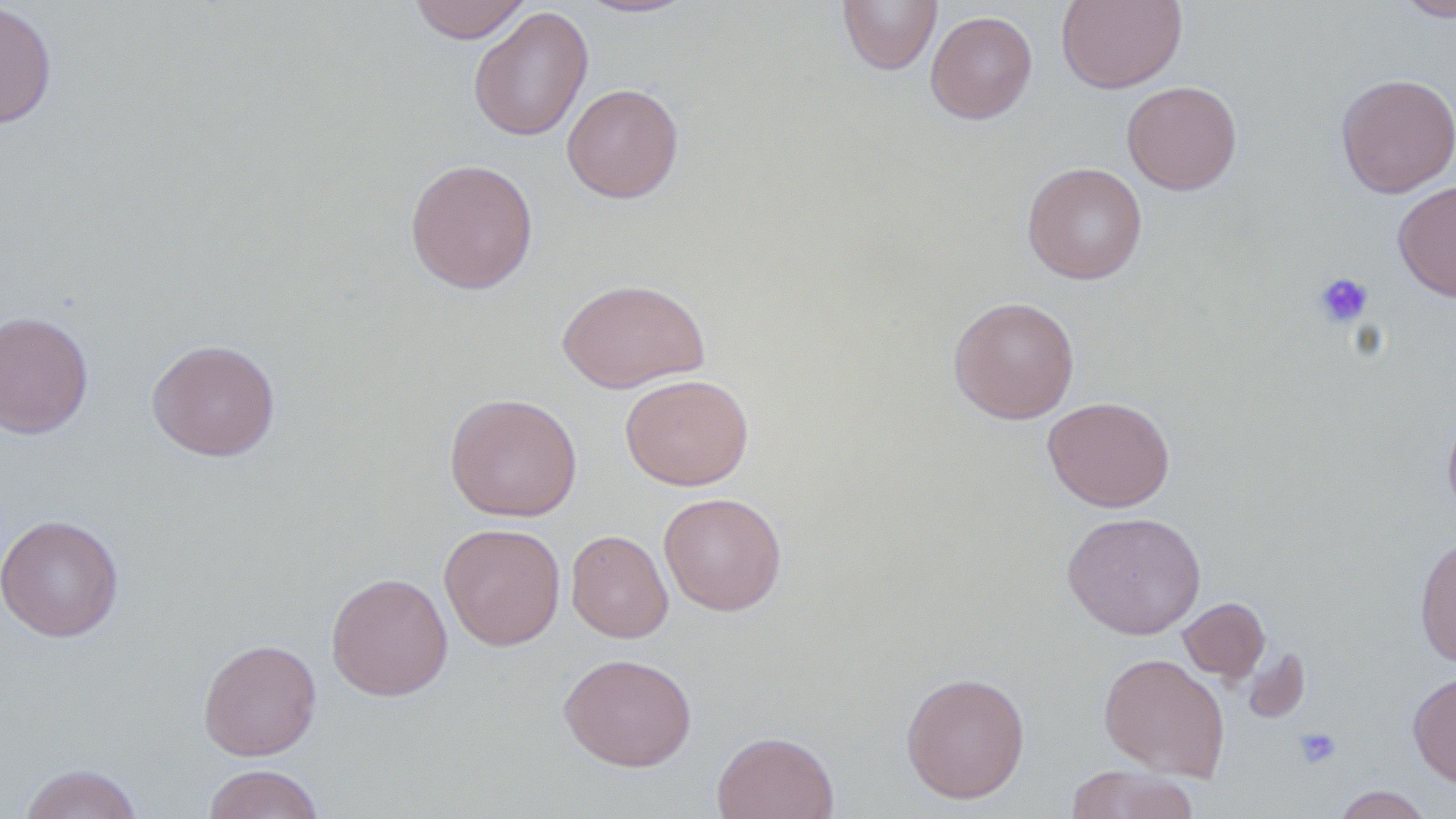 Approximate bounding boxes as named x1/y1/x2/y2 corners in pixels. Uninfected red blood cell locations: (x1=408, y1=0, x2=531, y2=43), (x1=574, y1=0, x2=699, y2=19), (x1=837, y1=0, x2=942, y2=75), (x1=1056, y1=0, x2=1187, y2=93), (x1=1396, y1=0, x2=1456, y2=22), (x1=0, y1=1, x2=57, y2=129), (x1=468, y1=6, x2=594, y2=142), (x1=925, y1=10, x2=1038, y2=124), (x1=1335, y1=73, x2=1456, y2=198), (x1=1122, y1=80, x2=1242, y2=195), (x1=562, y1=83, x2=684, y2=203), (x1=404, y1=158, x2=539, y2=294), (x1=1022, y1=162, x2=1147, y2=284), (x1=1393, y1=180, x2=1456, y2=302), (x1=557, y1=277, x2=710, y2=393), (x1=948, y1=296, x2=1080, y2=424), (x1=0, y1=311, x2=94, y2=438), (x1=146, y1=339, x2=281, y2=461), (x1=620, y1=373, x2=754, y2=491), (x1=444, y1=393, x2=582, y2=521), (x1=1043, y1=396, x2=1175, y2=513), (x1=1441, y1=404, x2=1456, y2=523), (x1=658, y1=492, x2=787, y2=616), (x1=1061, y1=511, x2=1207, y2=639), (x1=0, y1=514, x2=125, y2=641), (x1=439, y1=522, x2=566, y2=651), (x1=566, y1=529, x2=673, y2=643), (x1=1414, y1=534, x2=1456, y2=668), (x1=325, y1=572, x2=454, y2=701), (x1=1178, y1=597, x2=1270, y2=684), (x1=198, y1=638, x2=322, y2=761), (x1=1240, y1=646, x2=1311, y2=725), (x1=558, y1=652, x2=697, y2=771), (x1=1098, y1=652, x2=1230, y2=781), (x1=900, y1=670, x2=1031, y2=804), (x1=1408, y1=671, x2=1456, y2=788), (x1=711, y1=731, x2=839, y2=819), (x1=18, y1=763, x2=144, y2=819), (x1=202, y1=764, x2=326, y2=819), (x1=1064, y1=765, x2=1198, y2=819), (x1=1331, y1=785, x2=1434, y2=818). Platelet locations: (x1=1313, y1=272, x2=1374, y2=328), (x1=1294, y1=726, x2=1342, y2=769). Slide-level diagnosis: negative for blood parasites. Captured at 1000x magnification. May-Grünwald-Giemsa stain. Single field of view. Image is 1456×819 pixels. Thin blood smear. Light microscopy.